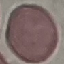
Summary:
  - Result: no malaria parasites seen
  - Image type: automatically extracted cell patch, resized to 64 × 64 pixels
  - Stain: Giemsa
  - Preparation: thin blood smear
  - Capture: smartphone camera at the microscope eyepiece